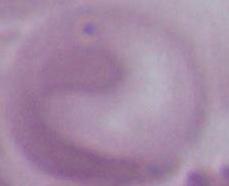
Summary:
  - Magnification: 1000x
  - Modality: photomicrograph
  - Identification: red blood cell